Comment on the morphology of the red blood cells.
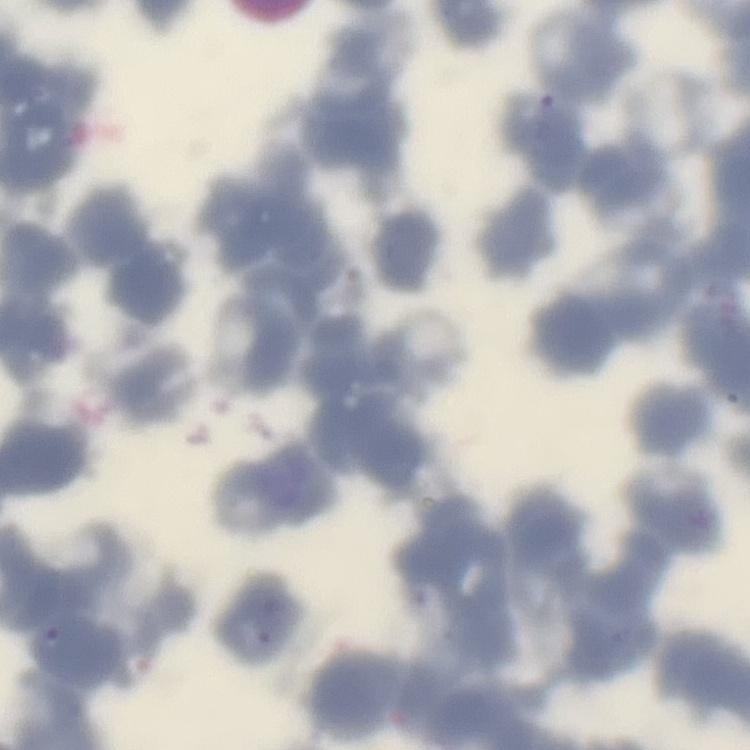

They show rouleaux formation.

Stained with either Field's or Giemsa. One tile cut from a larger photomicrograph. Thin peripheral smear.